Assess the morphology of the red blood cells.
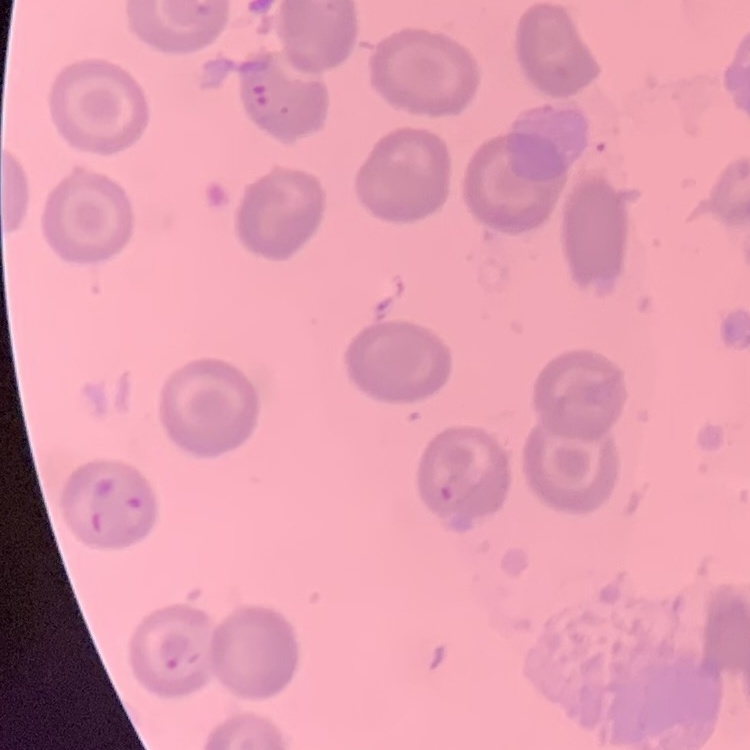

They show no rouleaux formation.

One tile cut from a larger photomicrograph. Thin peripheral smear. Field's or Giemsa stain.